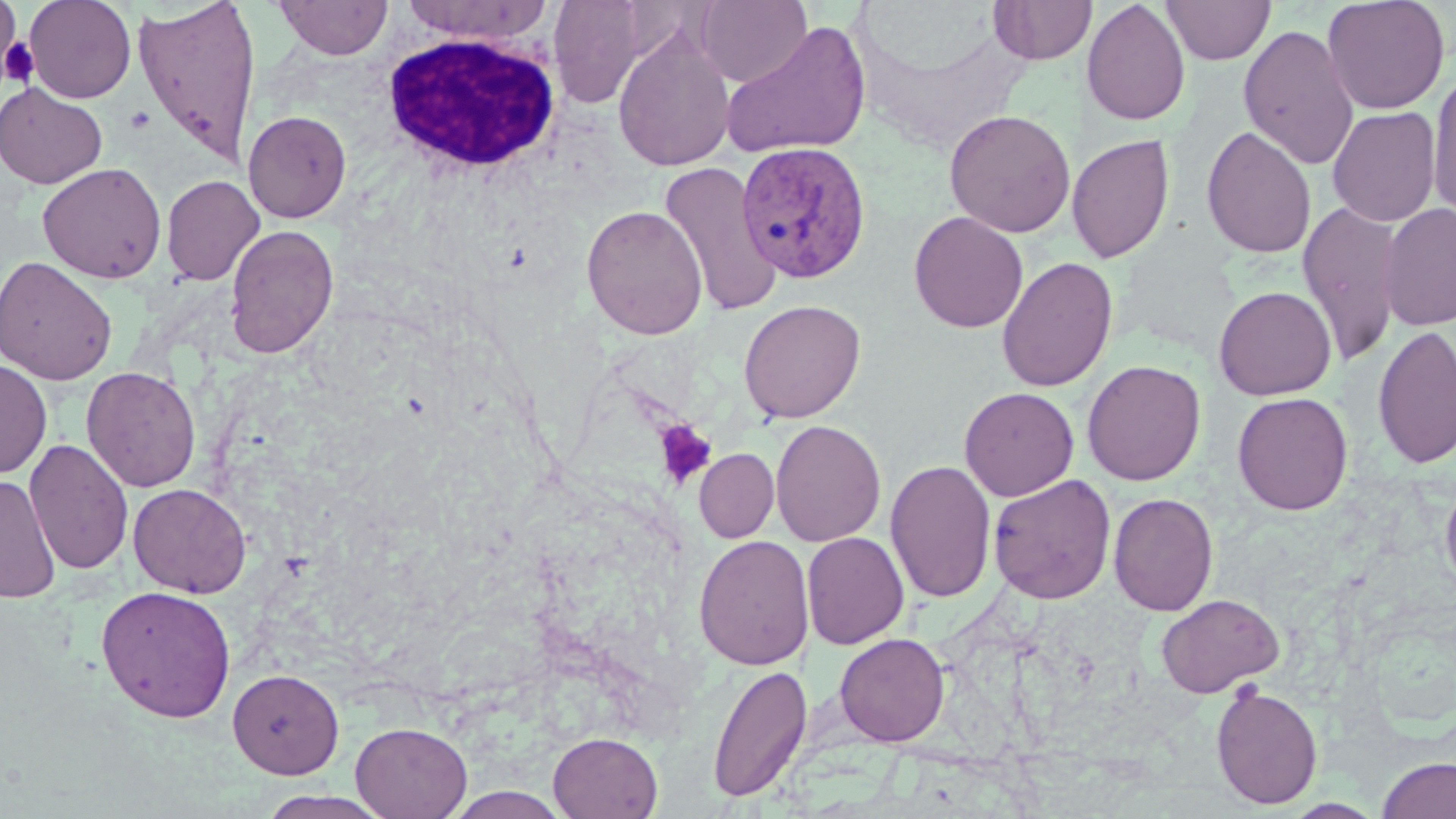

slide-level diagnosis = Plasmodium vivax
field of view = one of a larger specimen
image size = 1456×819 pixels
platelet locations = approximate bounding boxes as named x1/y1/x2/y2 corners in pixels: (x1=0, y1=38, x2=41, y2=89), (x1=124, y1=106, x2=156, y2=134), (x1=653, y1=419, x2=717, y2=490)
Plasmodium vivax-infected red blood cell locations = approximate bounding boxes as named x1/y1/x2/y2 corners in pixels: (x1=737, y1=140, x2=872, y2=285)
uninfected red blood cell locations = approximate bounding boxes as named x1/y1/x2/y2 corners in pixels: (x1=23, y1=0, x2=136, y2=103), (x1=275, y1=0, x2=393, y2=60), (x1=695, y1=0, x2=811, y2=86), (x1=1081, y1=0, x2=1190, y2=126), (x1=1161, y1=0, x2=1276, y2=65), (x1=1322, y1=0, x2=1450, y2=115), (x1=1, y1=1, x2=20, y2=77), (x1=131, y1=1, x2=262, y2=167), (x1=400, y1=1, x2=554, y2=43), (x1=547, y1=1, x2=649, y2=107), (x1=989, y1=1, x2=1096, y2=65), (x1=720, y1=19, x2=872, y2=160), (x1=1238, y1=24, x2=1360, y2=171), (x1=612, y1=26, x2=736, y2=173), (x1=1427, y1=66, x2=1456, y2=225), (x1=0, y1=83, x2=107, y2=189), (x1=1327, y1=106, x2=1441, y2=227), (x1=944, y1=109, x2=1076, y2=237), (x1=243, y1=110, x2=351, y2=223), (x1=1201, y1=125, x2=1317, y2=259), (x1=1066, y1=134, x2=1174, y2=264), (x1=659, y1=160, x2=782, y2=317), (x1=37, y1=162, x2=167, y2=283), (x1=161, y1=175, x2=265, y2=285), (x1=1297, y1=201, x2=1405, y2=369), (x1=1378, y1=203, x2=1456, y2=331), (x1=581, y1=205, x2=708, y2=339), (x1=909, y1=211, x2=1028, y2=333), (x1=224, y1=224, x2=339, y2=359), (x1=0, y1=256, x2=118, y2=385), (x1=996, y1=256, x2=1118, y2=392), (x1=1213, y1=285, x2=1336, y2=400), (x1=738, y1=299, x2=866, y2=423), (x1=1372, y1=325, x2=1456, y2=470), (x1=0, y1=358, x2=52, y2=479), (x1=1082, y1=360, x2=1206, y2=486), (x1=81, y1=366, x2=201, y2=491), (x1=959, y1=386, x2=1078, y2=501), (x1=1232, y1=391, x2=1353, y2=515), (x1=770, y1=419, x2=886, y2=546), (x1=24, y1=438, x2=134, y2=575), (x1=694, y1=448, x2=779, y2=542), (x1=885, y1=459, x2=997, y2=604), (x1=1440, y1=471, x2=1456, y2=597), (x1=987, y1=474, x2=1116, y2=604), (x1=0, y1=476, x2=61, y2=604), (x1=127, y1=482, x2=252, y2=598), (x1=1109, y1=492, x2=1219, y2=616), (x1=802, y1=532, x2=909, y2=650), (x1=693, y1=534, x2=815, y2=670), (x1=96, y1=585, x2=236, y2=723), (x1=1155, y1=593, x2=1284, y2=697), (x1=834, y1=632, x2=949, y2=746), (x1=706, y1=663, x2=813, y2=803), (x1=228, y1=668, x2=344, y2=778), (x1=1210, y1=682, x2=1323, y2=809), (x1=351, y1=721, x2=472, y2=819), (x1=548, y1=732, x2=663, y2=818), (x1=1377, y1=757, x2=1456, y2=819), (x1=255, y1=790, x2=394, y2=819)
stain = May-Grünwald-Giemsa
white blood cell locations = approximate bounding boxes as named x1/y1/x2/y2 corners in pixels: (x1=379, y1=29, x2=563, y2=174)
modality = optical microscopy
preparation = thin blood smear
magnification = 1000x